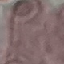
Result: negative for malaria parasites. Cell patch, automatically extracted from a larger field of view and resized to 64 × 64 pixels. Giemsa-stained preparation. Acquired by smartphone through the microscope eyepiece. Thin smear of blood.